Comment on the morphology of the erythrocytes.
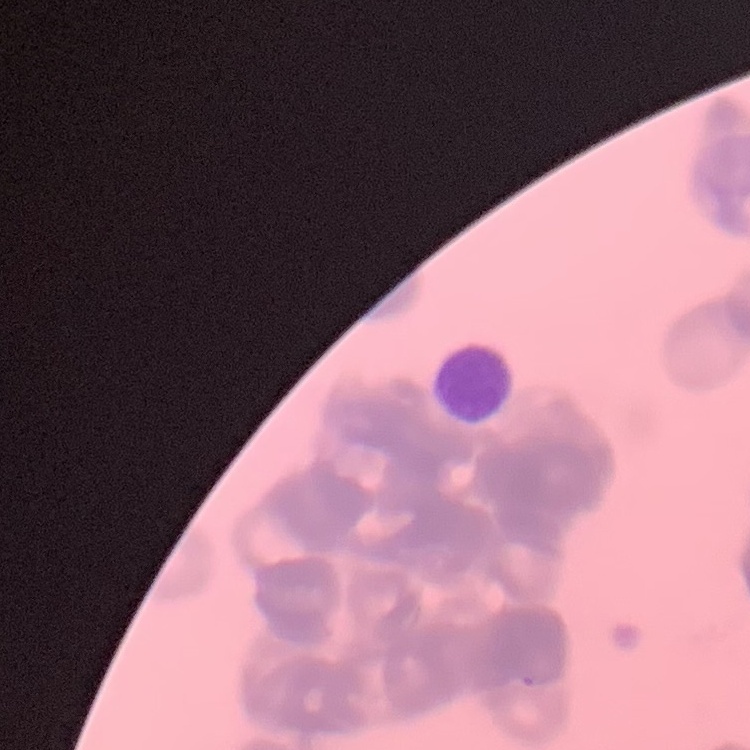
Rouleaux formation.

preparation = thin blood smear
stain = Field's or Giemsa
image type = square crop of a larger photomicrograph